Identify the preparation type.
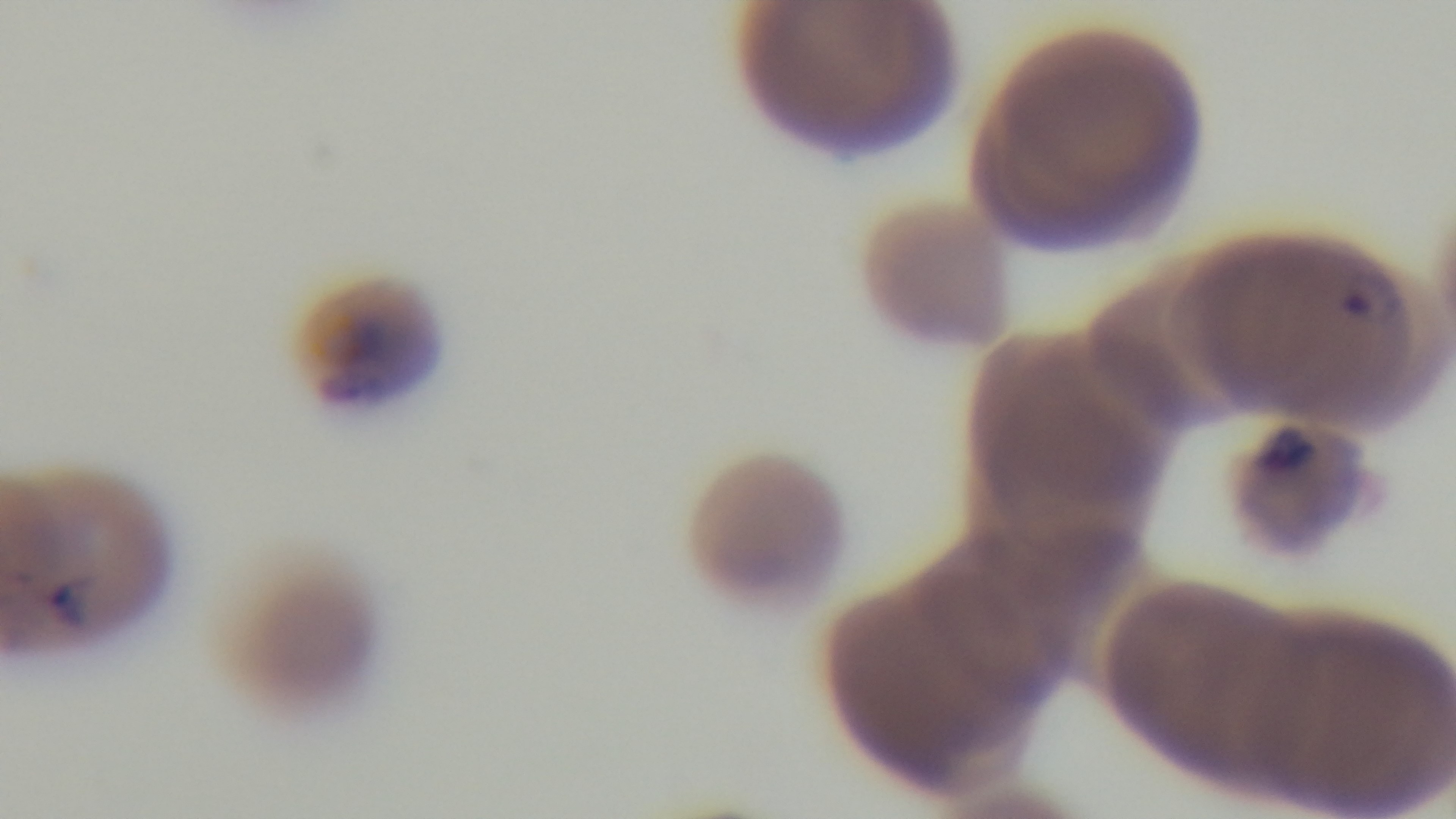

It is a thin blood film.

malaria status = infected
modality = light microscopy
field of view = single
capture = mounted 4K digital camera
objective = 100x oil immersion
stain = Giemsa